Point out every Plasmodium parasite and every leukocyte.
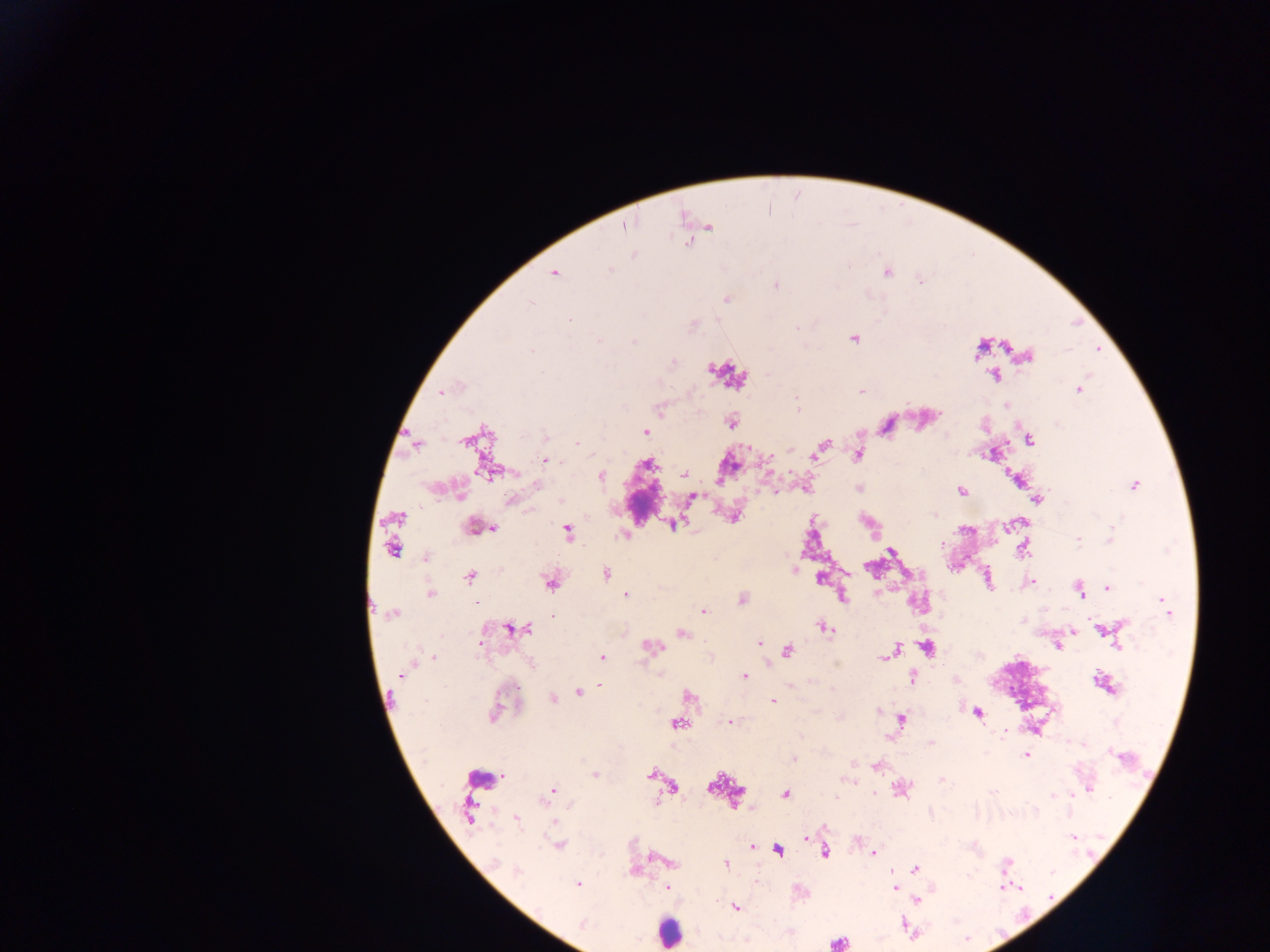

Approximate centers as [x, y] in pixels.
Plasmodium parasites: [625, 226], [709, 227], [634, 255], [610, 269], [554, 272], [887, 272], [920, 280], [776, 286], [726, 300], [531, 303], [570, 320], [692, 327], [854, 339], [634, 341], [531, 351], [1028, 357], [673, 362], [994, 375], [1079, 390], [861, 391], [442, 392], [797, 402], [1006, 406], [660, 408], [731, 422], [645, 432], [544, 436], [1029, 440], [578, 444], [415, 445], [822, 447], [790, 450], [858, 455], [545, 460], [647, 465], [488, 471], [684, 474], [601, 477], [1016, 479], [537, 485], [1133, 486], [961, 492], [692, 498], [511, 500], [560, 500], [1037, 500], [395, 518], [672, 524], [1008, 526], [477, 528], [490, 528], [568, 532], [1110, 539], [1078, 540], [942, 543], [392, 549], [1023, 549], [891, 551], [427, 557], [795, 569], [606, 574], [470, 576], [819, 579], [988, 580], [1032, 582], [550, 583], [1108, 588], [1079, 590], [430, 594], [626, 595], [843, 597], [742, 600], [1165, 605], [703, 611], [393, 614], [553, 617], [824, 627], [528, 628], [511, 629], [1104, 630], [682, 634], [760, 643], [1058, 646], [1119, 646], [651, 647], [927, 647], [788, 651], [894, 652], [888, 655], [433, 657], [603, 658], [532, 665], [401, 675], [745, 676], [913, 678], [1104, 683], [599, 686], [833, 688], [1110, 688], [579, 692], [688, 695], [552, 699], [772, 700], [494, 713], [978, 713], [902, 720], [730, 722], [677, 724], [1004, 732], [931, 743], [1027, 755], [794, 759], [875, 767], [650, 774], [595, 776], [942, 779], [848, 780], [673, 786], [1090, 788], [900, 789], [550, 793], [785, 794], [1053, 794], [1073, 794], [468, 811], [1035, 811], [516, 819], [554, 822], [807, 837], [1073, 837], [559, 845], [752, 847], [778, 851], [873, 853], [824, 854], [495, 862], [669, 862], [725, 864], [1006, 865], [914, 869], [518, 872], [577, 884], [667, 888], [894, 888], [1018, 888], [917, 901], [735, 907], [583, 924], [838, 943].
Leukocytes: [644, 502], [486, 776], [668, 932].

Summary:
  - Field of view: single
  - Preparation: thick blood smear
  - Image size: 1270×952 pixels
  - Country: Ghana
  - Capture: mobile-phone photograph through a microscope